Locate every Plasmodium falciparum-infected red blood cell.
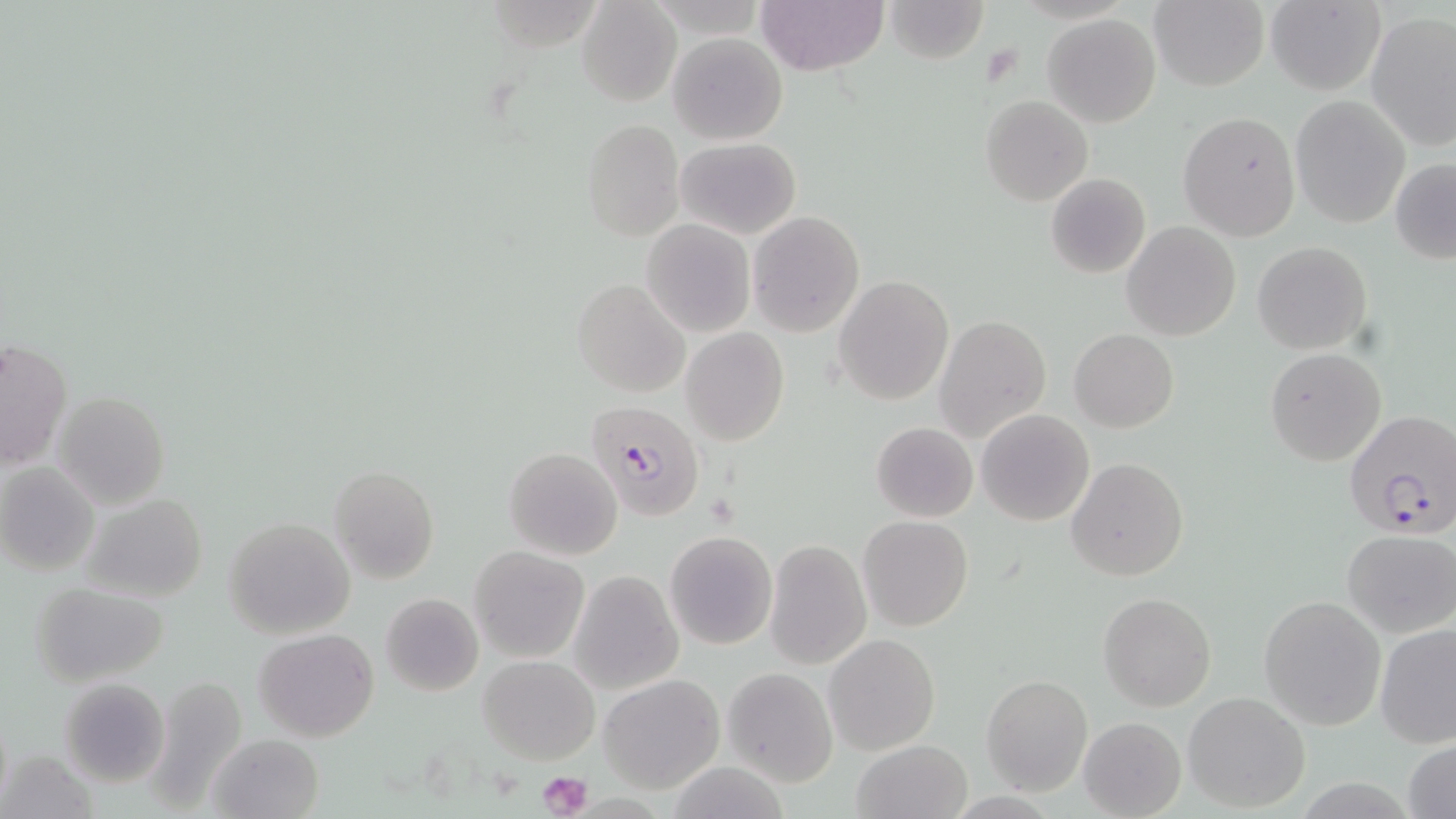

Approximate bounding boxes as (x1, y1, x2, y2) in pixels.
Plasmodium falciparum-infected red blood cells: (583, 399, 706, 521), (1344, 410, 1456, 540).

slide-level diagnosis = Plasmodium falciparum
modality = optical microscopy
magnification = 1000x
field of view = single
stain = May-Grünwald-Giemsa
preparation = thin blood smear
uninfected red blood cell locations = approximate bounding boxes as (x1, y1, x2, y2) in pixels: (757, 0, 886, 76), (1150, 0, 1270, 91), (577, 1, 680, 107), (884, 1, 988, 64), (1264, 1, 1386, 94), (1283, 7, 1452, 131), (1043, 12, 1161, 127), (1364, 12, 1456, 154), (667, 32, 787, 145), (980, 95, 1093, 207), (1290, 95, 1410, 228), (1177, 111, 1301, 240), (580, 117, 684, 240), (673, 137, 802, 238), (1390, 158, 1456, 265), (1045, 173, 1151, 279), (748, 211, 864, 337), (642, 221, 756, 337), (1122, 221, 1241, 341), (1252, 240, 1372, 354), (833, 275, 953, 405), (572, 278, 691, 397), (935, 315, 1051, 441), (681, 328, 789, 446), (1069, 328, 1179, 433), (1, 339, 72, 469), (1265, 348, 1386, 466), (52, 390, 171, 509), (976, 409, 1094, 526), (870, 422, 978, 522), (505, 447, 623, 560), (1066, 456, 1190, 582), (0, 462, 99, 577), (329, 466, 439, 583), (80, 492, 209, 604), (858, 515, 973, 633), (223, 518, 356, 638), (1340, 529, 1454, 638), (664, 530, 778, 649), (764, 538, 873, 670), (470, 545, 590, 662), (570, 570, 683, 693), (32, 581, 170, 687), (1099, 592, 1217, 710), (380, 593, 483, 697), (1259, 593, 1386, 730), (1375, 623, 1456, 748), (253, 628, 379, 743), (825, 634, 939, 754), (479, 655, 599, 764), (723, 667, 837, 787), (598, 673, 726, 793), (980, 675, 1093, 796), (59, 677, 169, 786), (142, 677, 247, 813), (1182, 691, 1310, 811), (1079, 717, 1186, 819), (209, 733, 324, 819), (850, 738, 974, 819), (1405, 738, 1456, 819), (2, 747, 98, 818)
platelet locations = approximate bounding boxes as (x1, y1, x2, y2) in pixels: (538, 770, 592, 819)
image size = 1456×819 pixels